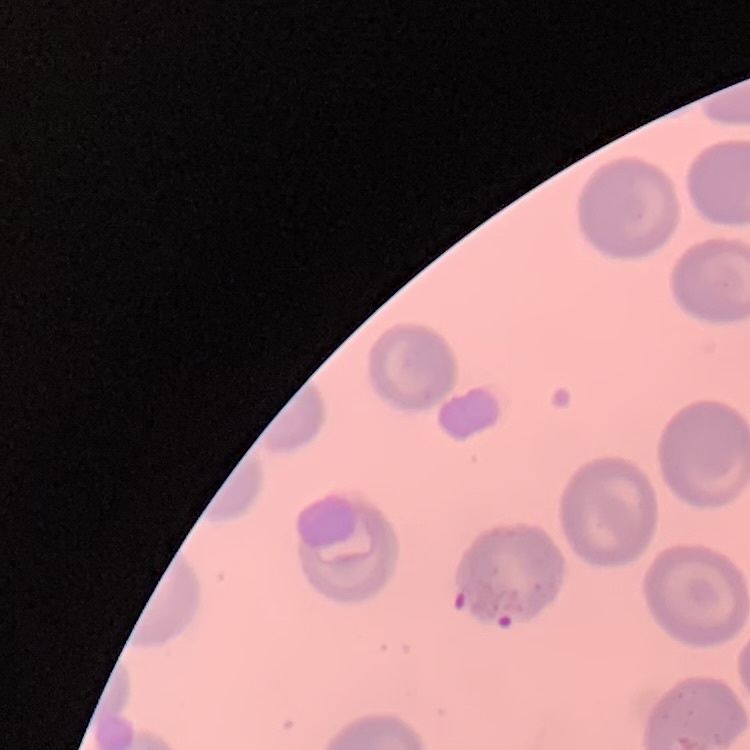 The erythrocytes show no rouleaux formation. Thin peripheral smear. One tile cut from a larger photomicrograph. Field's or Giemsa stain.